Comment on the morphology of the red blood cells.
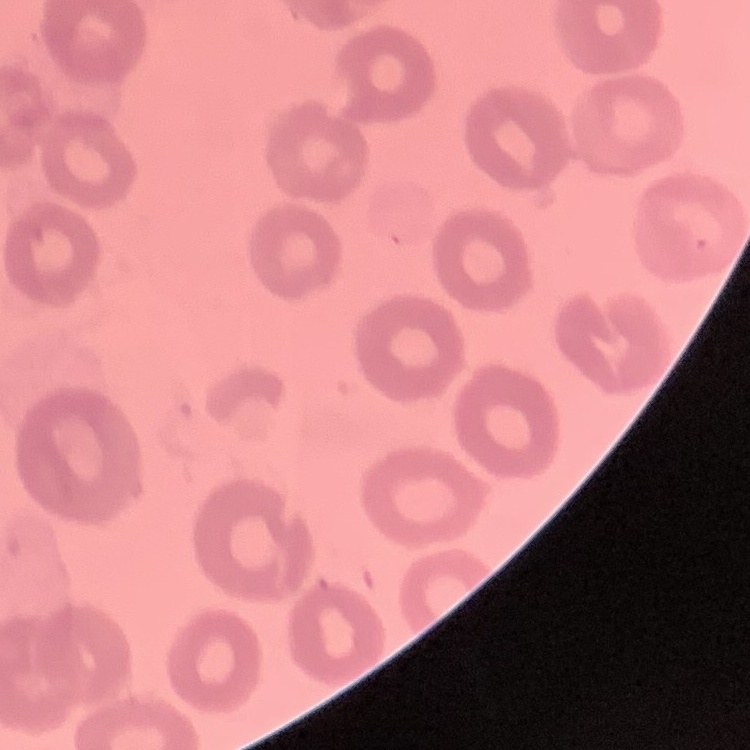
No rouleaux formation.

image type = one tile cut from a larger photomicrograph
preparation = thin blood smear
stain = Field's or Giemsa